Comment on the morphology of the erythrocytes.
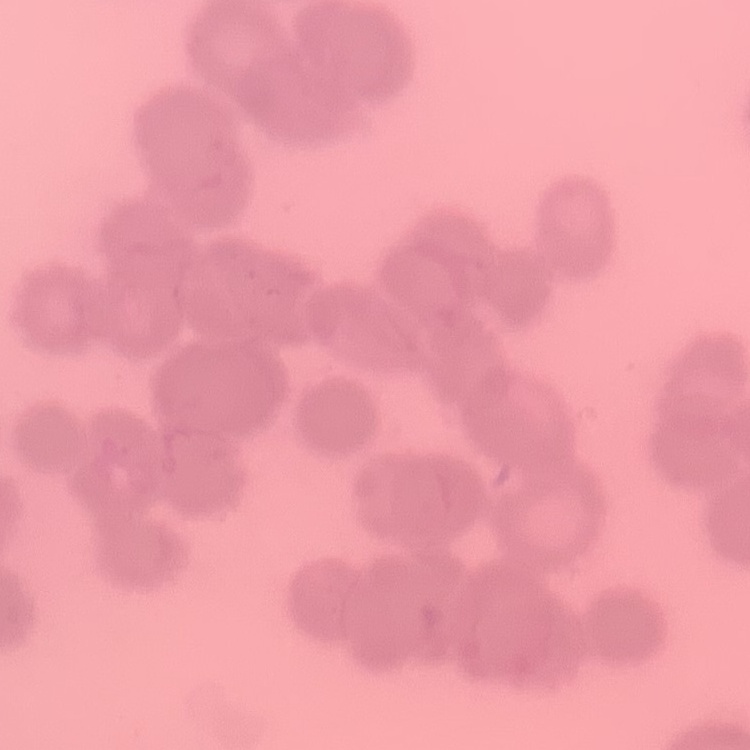
They show rouleaux formation.

Square crop of a larger photomicrograph. Field's or Giemsa stain. Thin blood film.